Classify this cell by malaria status.
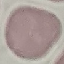

Uninfected.

Photographed with a smartphone camera at the microscope eyepiece. Automatically extracted cell patch, resized to 64 × 64 pixels. Thin blood film. Giemsa stain.